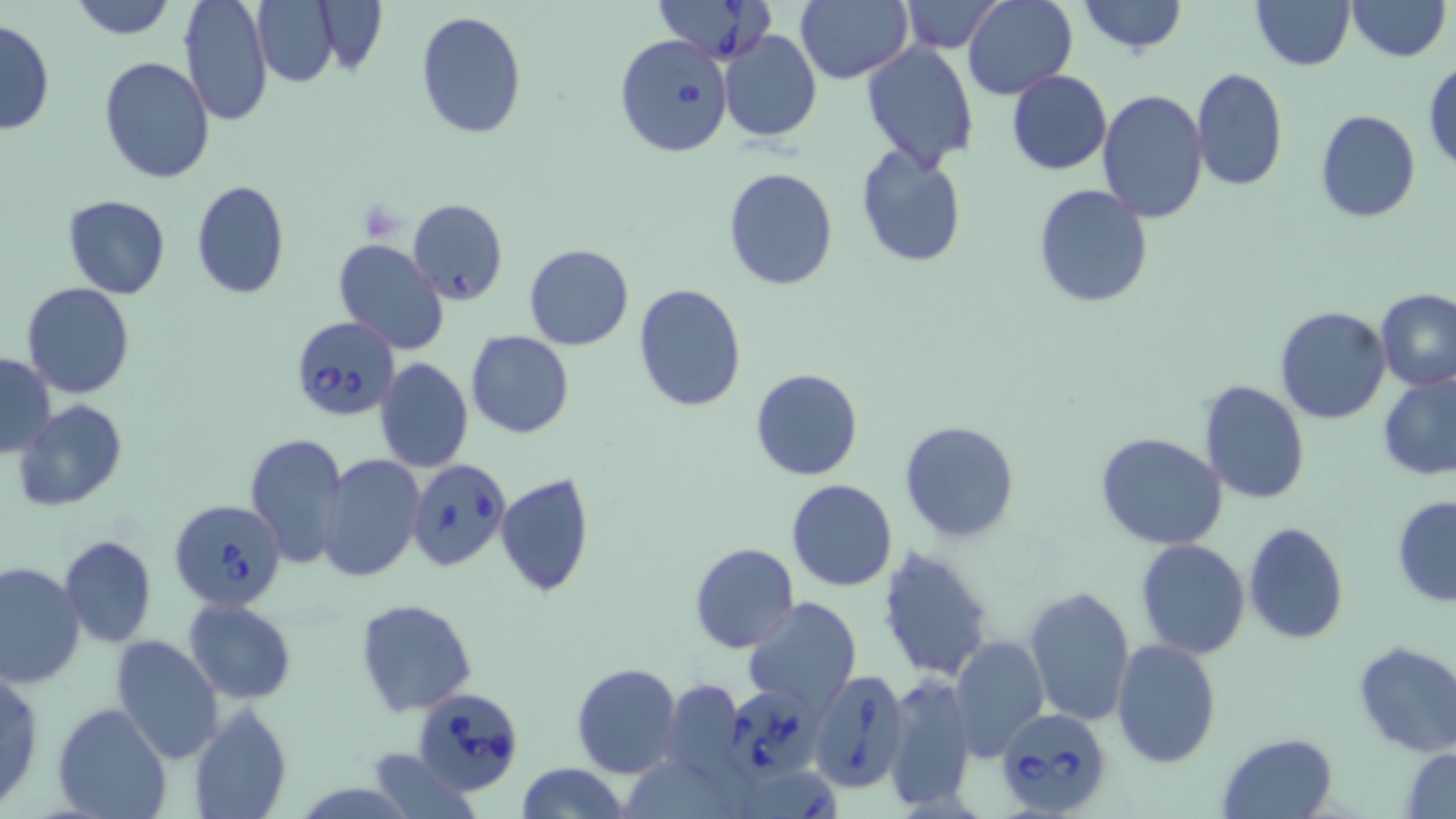
Summary:
  - Coordinate format: approximate bounding boxes as (x1, y1, x2, y2) in pixels
  - Platelet locations: (358, 200, 405, 241)
  - Babesia divergens-infected red blood cell locations: (653, 0, 778, 63), (614, 33, 733, 157), (407, 198, 507, 305), (289, 320, 404, 424), (407, 458, 512, 572), (171, 496, 288, 610), (807, 670, 908, 793), (725, 683, 821, 776), (410, 687, 524, 796), (996, 710, 1113, 814), (735, 767, 848, 819)
  - Uninfected red blood cell locations: (67, 0, 178, 39), (179, 0, 273, 125), (898, 0, 1004, 53), (961, 0, 1078, 101), (1076, 0, 1188, 54), (1346, 0, 1449, 62), (316, 1, 385, 76), (795, 1, 913, 84), (1251, 1, 1356, 71), (252, 2, 341, 86), (414, 10, 527, 142), (0, 18, 55, 136), (719, 30, 821, 143), (862, 42, 978, 169), (98, 56, 216, 184), (1424, 59, 1456, 171), (1191, 68, 1290, 193), (1006, 70, 1111, 176), (1097, 90, 1209, 225), (1314, 109, 1421, 223), (855, 144, 968, 268), (723, 167, 838, 290), (191, 180, 291, 300), (1031, 183, 1154, 309), (63, 194, 169, 299), (335, 238, 449, 355), (524, 244, 634, 349), (633, 283, 745, 413), (22, 284, 134, 400), (1377, 288, 1456, 393), (1274, 305, 1393, 424), (465, 330, 575, 438), (0, 351, 55, 457), (375, 358, 473, 472), (751, 369, 862, 481), (1378, 371, 1456, 481), (1198, 379, 1311, 504), (13, 400, 126, 512), (899, 419, 1021, 542), (1095, 432, 1228, 550), (244, 433, 349, 568), (319, 454, 425, 582), (495, 471, 596, 599), (787, 479, 898, 592), (1391, 496, 1456, 606), (1242, 521, 1351, 644), (60, 536, 156, 647), (1135, 539, 1251, 659), (688, 541, 800, 654), (876, 545, 995, 684), (1, 559, 84, 689), (1023, 585, 1136, 729), (743, 596, 862, 714), (356, 598, 475, 716), (184, 599, 297, 704), (949, 633, 1049, 759), (110, 635, 224, 763), (1110, 638, 1222, 768), (1353, 642, 1456, 757), (572, 663, 682, 779), (0, 668, 44, 811), (882, 674, 977, 811), (659, 679, 747, 783), (53, 702, 172, 819), (190, 702, 292, 819), (1217, 732, 1339, 819), (372, 747, 473, 818), (1403, 747, 1456, 817), (514, 763, 627, 819)
  - Slide-level diagnosis: Babesia divergens
  - Image size: 1456×819 pixels
  - Modality: optical microscopy
  - Preparation: thin blood film
  - Stain: May-Grünwald-Giemsa
  - Magnification: 1000x
  - Field of view: single